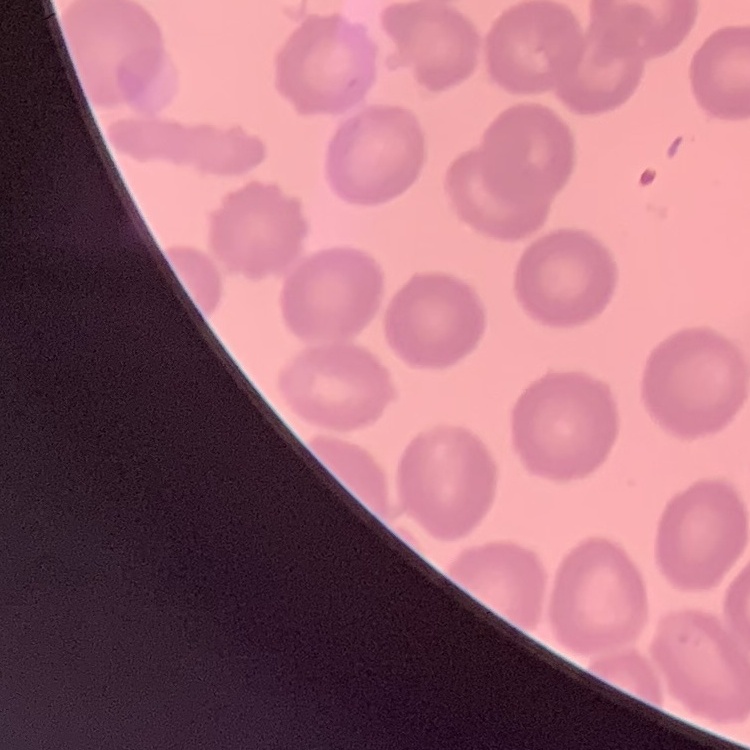
The erythrocytes exhibit no rouleaux formation. Field's or Giemsa stain. Thin peripheral smear. Square crop of a larger photomicrograph.